Classify this cell by malaria status.
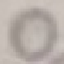

Uninfected.

Summary:
  - Preparation: thin smear
  - Capture: smartphone camera at the microscope eyepiece
  - Image type: cell patch, automatically extracted from a larger field of view and resized to 64 × 64 pixels
  - Stain: Giemsa